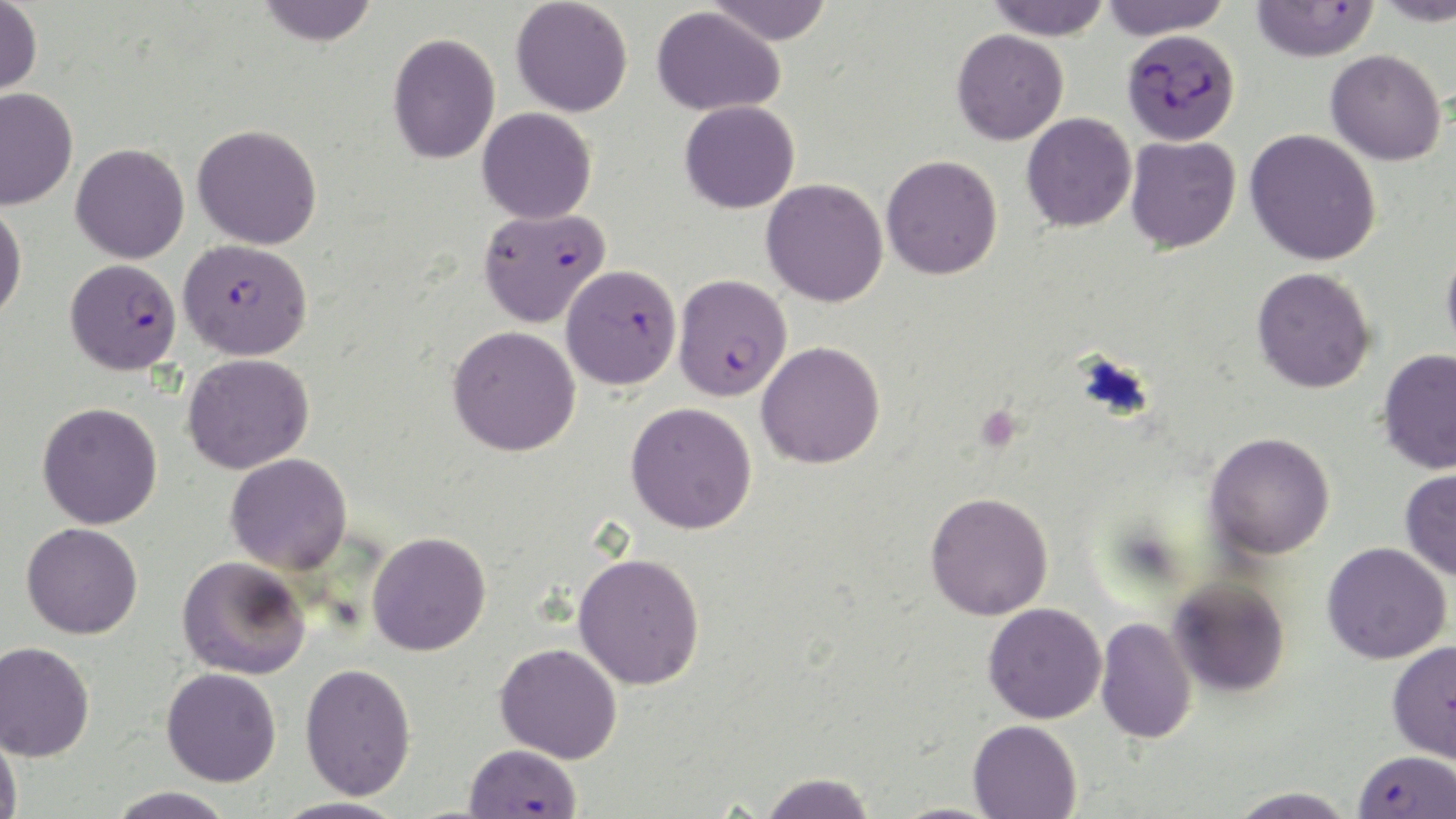
Plasmodium falciparum-infected red blood cell locations = approximate bounding boxes as (x1,y1)-(x2,y2) corner pairs in pixels: (1250,1)-(1379,62), (1122,29)-(1240,145), (478,207)-(610,328), (178,238)-(313,361), (65,258)-(181,375), (561,264)-(682,390), (673,274)-(792,401), (1387,639)-(1456,764), (464,744)-(583,817), (1353,749)-(1456,818)
slide-level diagnosis = Plasmodium falciparum
magnification = 1000x
platelet locations = approximate bounding boxes as (x1,y1)-(x2,y2) corner pairs in pixels: (976,405)-(1022,452)
uninfected red blood cell locations = approximate bounding boxes as (x1,y1)-(x2,y2) corner pairs in pixels: (0,0)-(42,99), (511,0)-(633,117), (704,0)-(835,45), (1100,0)-(1233,40), (1374,0)-(1455,26), (256,1)-(379,46), (985,1)-(1113,39), (651,5)-(786,116), (951,29)-(1068,145), (387,32)-(500,164), (1325,49)-(1446,166), (0,86)-(78,210), (679,100)-(800,214), (477,107)-(597,224), (1021,112)-(1137,232), (192,124)-(322,249), (1245,129)-(1382,266), (1125,135)-(1241,253), (71,143)-(189,264), (881,154)-(1003,280), (761,178)-(889,307), (0,203)-(27,324), (1442,240)-(1456,367), (1252,267)-(1376,393), (448,325)-(581,456), (756,341)-(885,469), (1378,348)-(1456,475), (183,353)-(314,474), (37,402)-(163,529), (625,402)-(757,534), (1205,431)-(1335,560), (226,453)-(352,574), (1400,468)-(1456,581), (925,491)-(1053,620), (21,523)-(143,639), (367,531)-(491,656), (1322,542)-(1452,664), (573,552)-(706,689), (177,555)-(310,679), (1168,575)-(1291,697), (983,602)-(1107,724), (1095,617)-(1198,744), (0,640)-(95,761), (494,642)-(623,763), (300,662)-(416,800), (161,667)-(282,787), (968,719)-(1081,819), (0,730)-(23,818), (759,772)-(877,818), (106,786)-(238,818), (1227,786)-(1358,819), (271,796)-(409,819)
stain = May-Grünwald-Giemsa
modality = optical microscopy
field of view = one of a larger specimen
image size = 1456×819 pixels
preparation = thin blood smear